Outline each blood parasite and name the species.
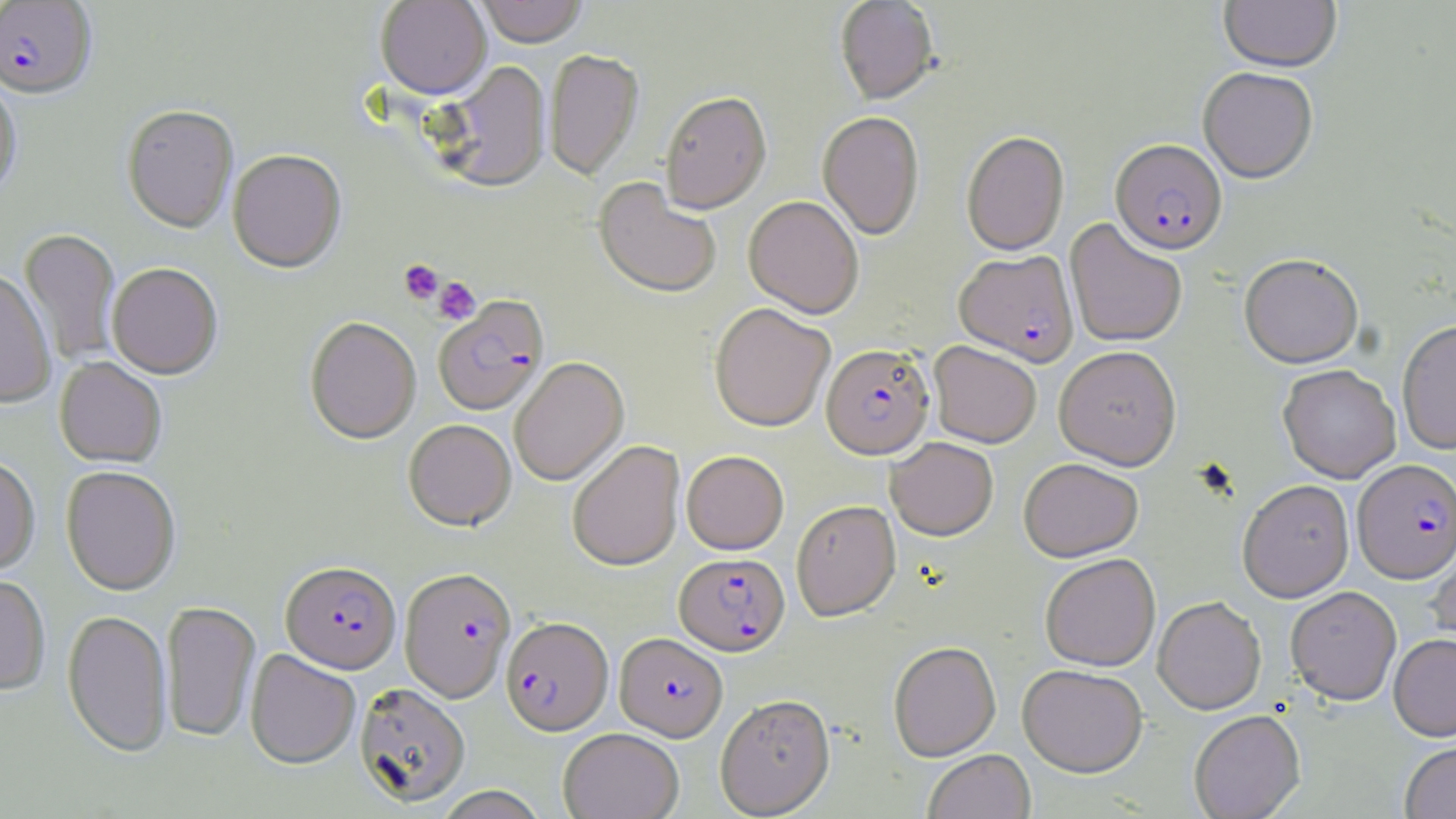
Approximate bounding boxes as named x1/y1/x2/y2 corners in pixels.
Plasmodium falciparum-infected red blood cells: (x1=0, y1=1, x2=97, y2=100), (x1=1110, y1=139, x2=1227, y2=254), (x1=954, y1=249, x2=1079, y2=366), (x1=434, y1=298, x2=549, y2=416), (x1=821, y1=344, x2=934, y2=459), (x1=1353, y1=459, x2=1456, y2=583), (x1=674, y1=552, x2=790, y2=656), (x1=280, y1=561, x2=401, y2=674), (x1=399, y1=567, x2=517, y2=703), (x1=501, y1=618, x2=613, y2=736), (x1=615, y1=633, x2=727, y2=741).
No Plasmodium ovale, Plasmodium malariae, Plasmodium vivax, Babesia divergens, or Trypanosoma brucei observed.

slide-level diagnosis = Plasmodium falciparum
field of view = single
image size = 1456×819 pixels
modality = light microscopy
stain = May-Grünwald-Giemsa
magnification = 1000x
uninfected red blood cell locations = approximate bounding boxes as named x1/y1/x2/y2 corners in pixels: (x1=375, y1=0, x2=491, y2=102), (x1=476, y1=0, x2=587, y2=49), (x1=834, y1=0, x2=939, y2=106), (x1=1219, y1=0, x2=1342, y2=73), (x1=544, y1=50, x2=644, y2=181), (x1=433, y1=62, x2=551, y2=194), (x1=1198, y1=66, x2=1318, y2=183), (x1=0, y1=79, x2=21, y2=201), (x1=660, y1=92, x2=771, y2=216), (x1=122, y1=106, x2=238, y2=234), (x1=817, y1=112, x2=925, y2=240), (x1=961, y1=131, x2=1069, y2=256), (x1=228, y1=150, x2=346, y2=274), (x1=593, y1=179, x2=721, y2=300), (x1=743, y1=195, x2=864, y2=318), (x1=1065, y1=218, x2=1187, y2=348), (x1=20, y1=228, x2=121, y2=366), (x1=1239, y1=254, x2=1364, y2=368), (x1=107, y1=263, x2=222, y2=380), (x1=0, y1=270, x2=57, y2=408), (x1=709, y1=303, x2=835, y2=432), (x1=304, y1=317, x2=421, y2=445), (x1=1397, y1=320, x2=1455, y2=453), (x1=929, y1=341, x2=1041, y2=448), (x1=1054, y1=346, x2=1182, y2=470), (x1=55, y1=357, x2=166, y2=468), (x1=509, y1=358, x2=629, y2=487), (x1=1278, y1=364, x2=1401, y2=482), (x1=404, y1=420, x2=516, y2=531), (x1=886, y1=437, x2=998, y2=540), (x1=567, y1=440, x2=685, y2=572), (x1=681, y1=450, x2=789, y2=554), (x1=0, y1=456, x2=40, y2=576), (x1=1019, y1=457, x2=1143, y2=562), (x1=61, y1=467, x2=180, y2=596), (x1=1237, y1=480, x2=1354, y2=601), (x1=791, y1=499, x2=900, y2=621), (x1=1427, y1=544, x2=1456, y2=658), (x1=1040, y1=554, x2=1160, y2=671), (x1=0, y1=574, x2=51, y2=696), (x1=1285, y1=586, x2=1401, y2=705), (x1=1152, y1=597, x2=1266, y2=714), (x1=161, y1=601, x2=261, y2=743), (x1=62, y1=610, x2=172, y2=758), (x1=1388, y1=633, x2=1456, y2=741), (x1=888, y1=641, x2=1001, y2=761), (x1=245, y1=650, x2=360, y2=770), (x1=1018, y1=664, x2=1147, y2=777), (x1=354, y1=683, x2=471, y2=807), (x1=715, y1=694, x2=835, y2=817), (x1=1189, y1=710, x2=1305, y2=819), (x1=559, y1=728, x2=683, y2=819), (x1=1400, y1=741, x2=1456, y2=819), (x1=923, y1=749, x2=1035, y2=819), (x1=434, y1=786, x2=548, y2=819)
preparation = thin blood film
platelet locations = approximate bounding boxes as named x1/y1/x2/y2 corners in pixels: (x1=399, y1=259, x2=444, y2=304), (x1=433, y1=277, x2=481, y2=325)